Give the extent of all uninfected red blood cells.
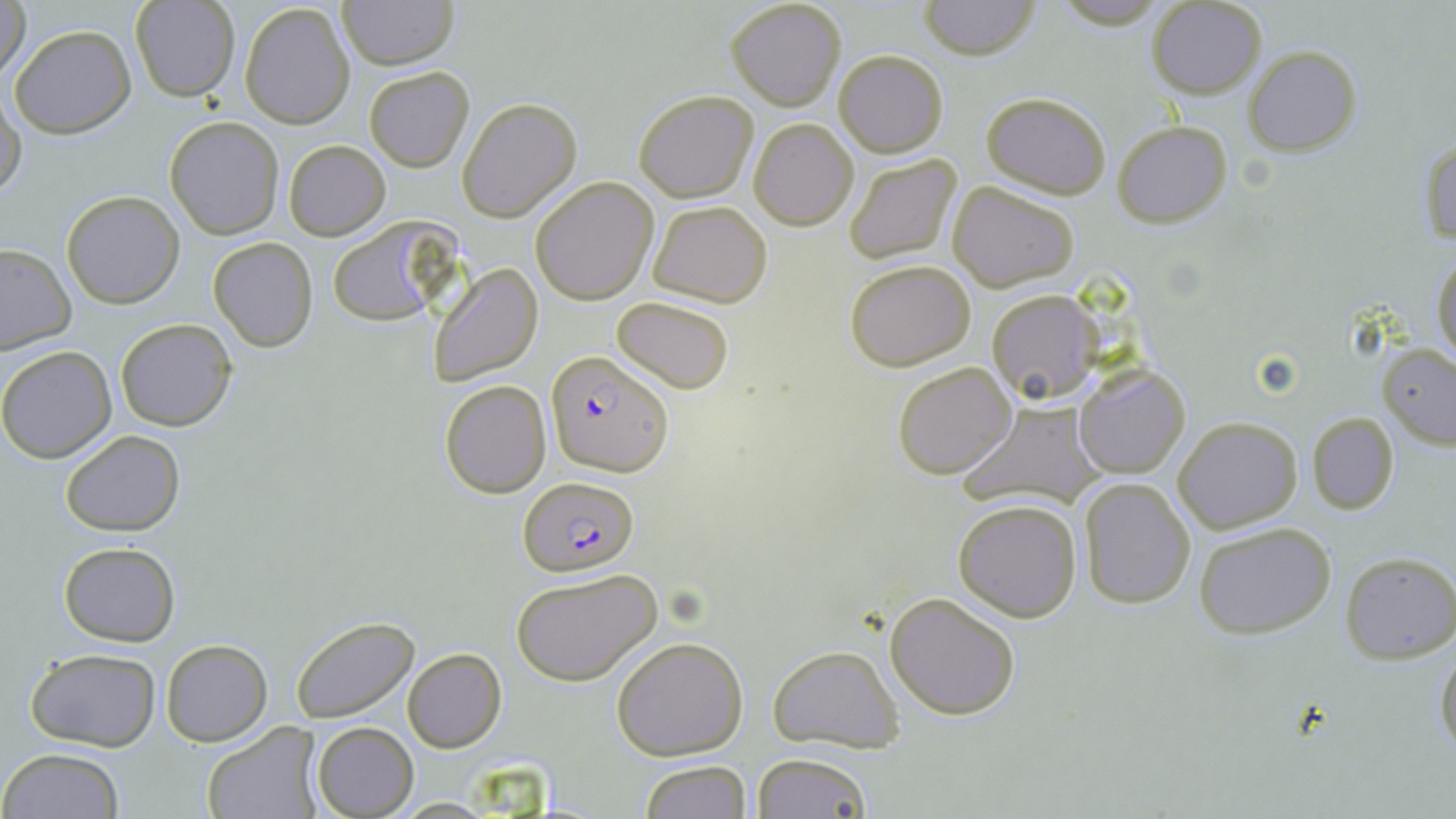

Approximate bounding boxes as (x1,y1)-(x2,y2) corner pairs in pixels.
Uninfected red blood cells: (0,0)-(29,83), (336,0)-(459,70), (918,0)-(1041,60), (132,1)-(240,102), (725,1)-(848,111), (1147,1)-(1266,98), (240,2)-(356,130), (7,24)-(137,137), (1243,45)-(1360,157), (834,49)-(948,157), (364,66)-(473,171), (0,89)-(27,201), (633,91)-(758,203), (980,91)-(1111,198), (456,96)-(582,223), (164,116)-(283,239), (748,118)-(859,230), (1111,119)-(1233,227), (1419,139)-(1455,247), (283,140)-(390,240), (843,154)-(963,266), (529,176)-(659,304), (947,182)-(1079,291), (61,190)-(185,309), (647,200)-(772,307), (325,217)-(456,328), (208,237)-(317,352), (0,243)-(73,355), (1430,250)-(1455,367), (844,258)-(976,370), (428,263)-(543,386), (986,289)-(1100,404), (612,296)-(737,394), (115,318)-(237,432), (1377,342)-(1456,450), (0,346)-(117,463), (892,361)-(1018,479), (1075,364)-(1190,479), (439,380)-(551,498), (961,399)-(1104,509), (1307,410)-(1399,515), (1174,418)-(1302,534), (60,429)-(186,536), (1078,477)-(1195,608), (953,498)-(1082,622), (1194,523)-(1336,639), (58,541)-(180,646), (1340,551)-(1456,663), (510,566)-(663,687), (885,590)-(1021,720), (291,616)-(419,722), (610,635)-(750,760), (160,640)-(272,747), (1435,641)-(1456,761), (767,644)-(903,753), (26,648)-(160,750), (402,649)-(506,752), (201,721)-(322,819), (312,721)-(418,818), (3,748)-(124,819), (753,753)-(872,819), (639,761)-(751,818), (392,797)-(504,818).

{
  "slide_level_diagnosis": "Plasmodium falciparum",
  "modality": "light microscopy",
  "plasmodium_falciparum_infected_red_blood_cell_locations": "approximate bounding boxes as (x1,y1)-(x2,y2) corner pairs in pixels: (544,350)-(673,476), (517,479)-(639,577)",
  "preparation": "thin blood film",
  "field_of_view": "one of a larger specimen",
  "magnification": "1000x",
  "image_size": "1456×819 pixels",
  "stain": "May-Grünwald-Giemsa"
}